Assess this cell for malaria.
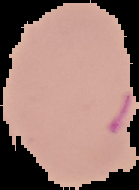
It is uninfected.

Summary:
  - Image size: 139×190 pixels
  - Image type: segmented cell region on a black background
  - Preparation: thin blood smear